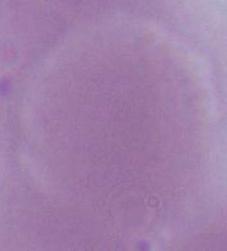
1000x magnification. An erythrocyte is shown. Micrograph.